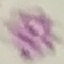

Summary:
  - Malaria status: uninfected
  - Image type: automatically extracted cell patch, resized to 64 × 64 pixels
  - Preparation: thin blood smear
  - Capture: smartphone camera at the microscope eyepiece
  - Stain: Giemsa